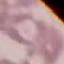

Malaria status: uninfected. Photographed with a smartphone camera at the microscope eyepiece. Giemsa stain. Thin blood film. Cell patch, automatically extracted from a larger field of view and resized to 64 × 64 pixels.